Comment on the morphology of the red blood cells.
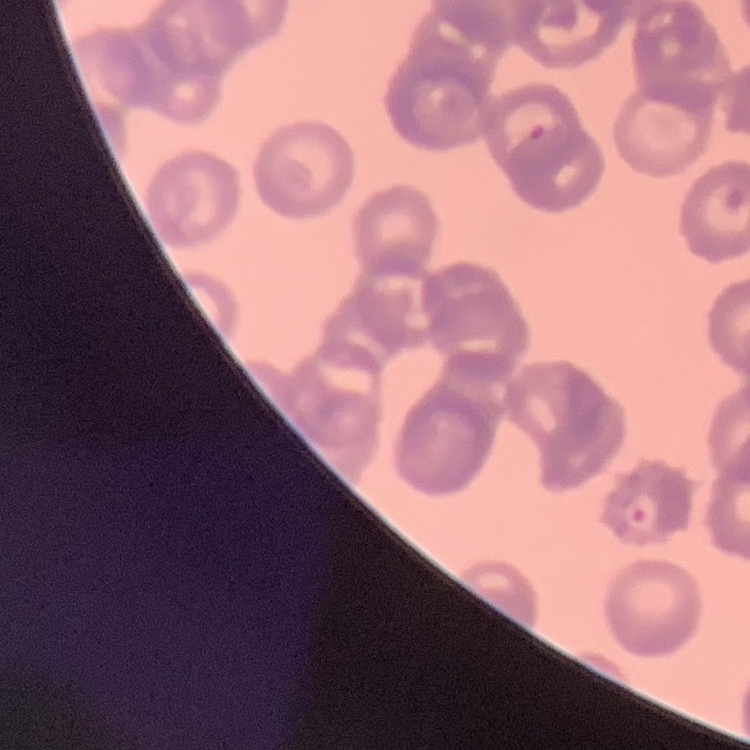

Rouleaux formation.

preparation: thin blood film
stain: Field's or Giemsa
image_type: one tile cut from a larger photomicrograph